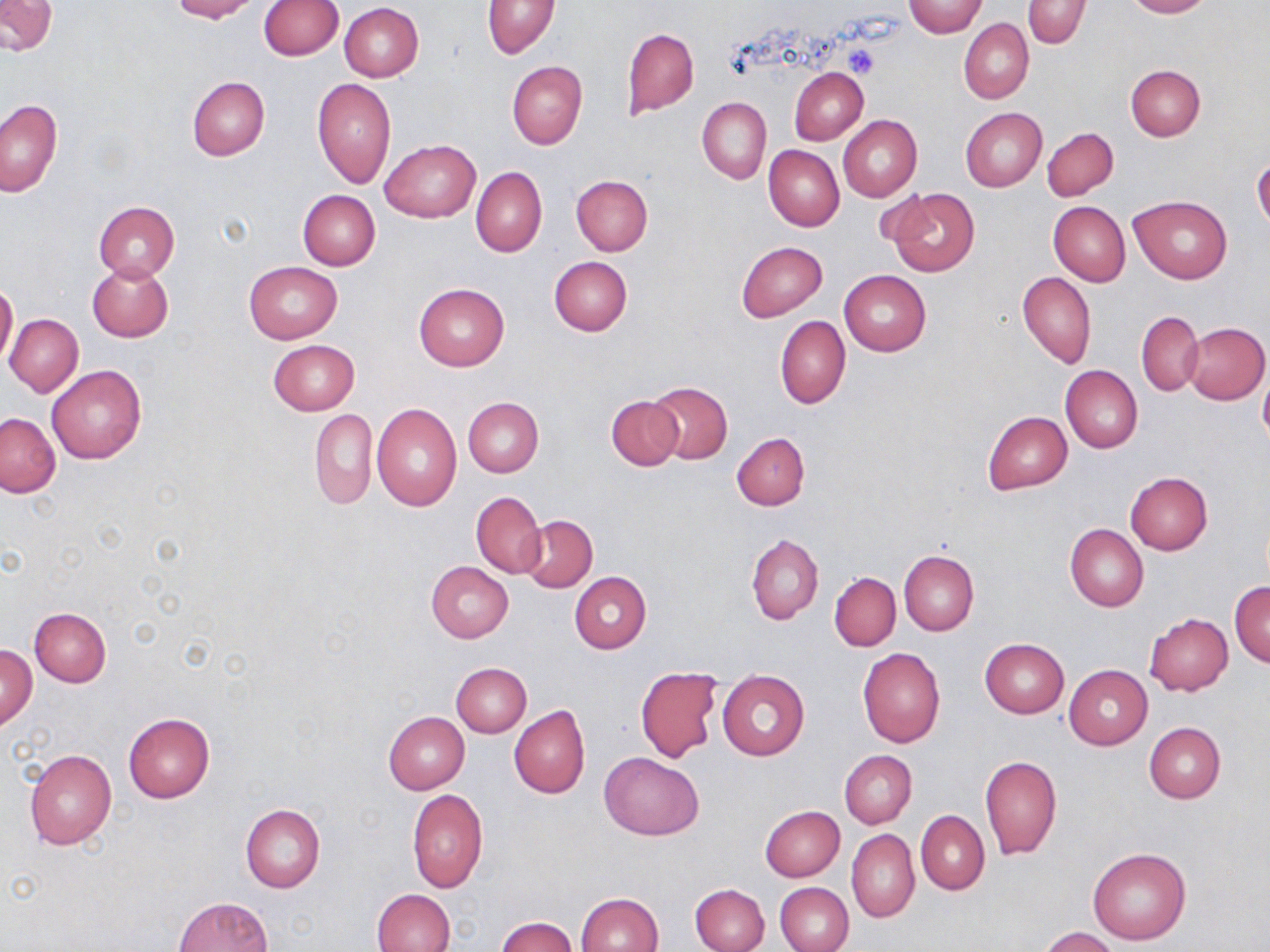

slide-level diagnosis = negative for blood parasites
field of view = single
magnification = 1000x
preparation = thin blood smear
modality = light microscopy
stain = May-Grünwald-Giemsa
platelet locations = approximate bounding boxes as named x1/y1/x2/y2 corners in pixels: (x1=844, y1=44, x2=880, y2=79)
image size = 1270×952 pixels
uninfected red blood cell locations = approximate bounding boxes as named x1/y1/x2/y2 corners in pixels: (x1=169, y1=0, x2=260, y2=21), (x1=260, y1=0, x2=343, y2=60), (x1=905, y1=0, x2=984, y2=37), (x1=1022, y1=0, x2=1090, y2=49), (x1=1122, y1=0, x2=1211, y2=18), (x1=1, y1=1, x2=57, y2=55), (x1=483, y1=1, x2=559, y2=59), (x1=340, y1=4, x2=424, y2=82), (x1=958, y1=19, x2=1033, y2=104), (x1=621, y1=27, x2=699, y2=117), (x1=507, y1=60, x2=588, y2=149), (x1=1124, y1=64, x2=1206, y2=141), (x1=790, y1=68, x2=868, y2=144), (x1=187, y1=76, x2=269, y2=160), (x1=312, y1=79, x2=395, y2=189), (x1=697, y1=96, x2=771, y2=184), (x1=0, y1=98, x2=61, y2=196), (x1=961, y1=108, x2=1047, y2=192), (x1=838, y1=114, x2=922, y2=202), (x1=1043, y1=127, x2=1118, y2=201), (x1=381, y1=139, x2=480, y2=223), (x1=764, y1=145, x2=844, y2=231), (x1=1252, y1=158, x2=1270, y2=231), (x1=471, y1=166, x2=546, y2=257), (x1=571, y1=175, x2=652, y2=256), (x1=885, y1=186, x2=980, y2=279), (x1=296, y1=189, x2=381, y2=270), (x1=1128, y1=196, x2=1232, y2=285), (x1=94, y1=201, x2=179, y2=281), (x1=1049, y1=201, x2=1130, y2=285), (x1=736, y1=241, x2=827, y2=322), (x1=549, y1=256, x2=633, y2=335), (x1=88, y1=262, x2=173, y2=342), (x1=243, y1=262, x2=342, y2=344), (x1=838, y1=270, x2=931, y2=356), (x1=1018, y1=272, x2=1097, y2=368), (x1=0, y1=281, x2=18, y2=370), (x1=414, y1=283, x2=509, y2=372), (x1=1136, y1=312, x2=1205, y2=394), (x1=4, y1=313, x2=83, y2=397), (x1=775, y1=316, x2=850, y2=409), (x1=1185, y1=321, x2=1269, y2=405), (x1=268, y1=340, x2=359, y2=415), (x1=46, y1=364, x2=146, y2=463), (x1=1060, y1=365, x2=1143, y2=453), (x1=1259, y1=371, x2=1270, y2=445), (x1=647, y1=381, x2=732, y2=464), (x1=607, y1=395, x2=684, y2=470), (x1=464, y1=397, x2=543, y2=476), (x1=371, y1=403, x2=462, y2=511), (x1=309, y1=408, x2=377, y2=510), (x1=983, y1=411, x2=1072, y2=494), (x1=0, y1=413, x2=61, y2=497), (x1=732, y1=432, x2=809, y2=510), (x1=1125, y1=471, x2=1213, y2=554), (x1=471, y1=492, x2=546, y2=579), (x1=520, y1=514, x2=598, y2=593), (x1=1065, y1=524, x2=1148, y2=611), (x1=747, y1=533, x2=824, y2=624), (x1=899, y1=551, x2=979, y2=636), (x1=426, y1=560, x2=514, y2=642), (x1=569, y1=571, x2=651, y2=653), (x1=829, y1=571, x2=900, y2=651), (x1=1229, y1=582, x2=1270, y2=667), (x1=29, y1=606, x2=111, y2=686), (x1=1143, y1=613, x2=1233, y2=696), (x1=980, y1=638, x2=1069, y2=718), (x1=2, y1=644, x2=37, y2=729), (x1=857, y1=647, x2=945, y2=747), (x1=451, y1=662, x2=532, y2=737), (x1=1064, y1=665, x2=1152, y2=749), (x1=636, y1=667, x2=721, y2=763), (x1=718, y1=669, x2=809, y2=760), (x1=510, y1=704, x2=590, y2=799), (x1=384, y1=711, x2=469, y2=793), (x1=123, y1=713, x2=215, y2=802), (x1=1144, y1=722, x2=1225, y2=803), (x1=23, y1=748, x2=117, y2=850), (x1=838, y1=750, x2=916, y2=828), (x1=600, y1=751, x2=703, y2=839), (x1=980, y1=755, x2=1062, y2=860), (x1=407, y1=789, x2=487, y2=893), (x1=240, y1=805, x2=324, y2=892), (x1=760, y1=805, x2=845, y2=882), (x1=916, y1=810, x2=989, y2=894), (x1=847, y1=829, x2=919, y2=923), (x1=1087, y1=847, x2=1190, y2=945), (x1=776, y1=882, x2=853, y2=952), (x1=690, y1=883, x2=769, y2=952), (x1=372, y1=888, x2=455, y2=952), (x1=577, y1=892, x2=664, y2=952), (x1=174, y1=897, x2=271, y2=952), (x1=498, y1=917, x2=577, y2=952), (x1=1039, y1=927, x2=1120, y2=952)